Identify the cell.
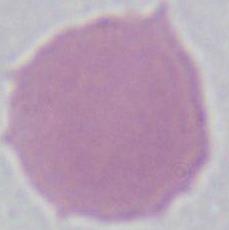
An erythrocyte.

Summary:
  - Magnification: 1000x
  - Modality: micrograph